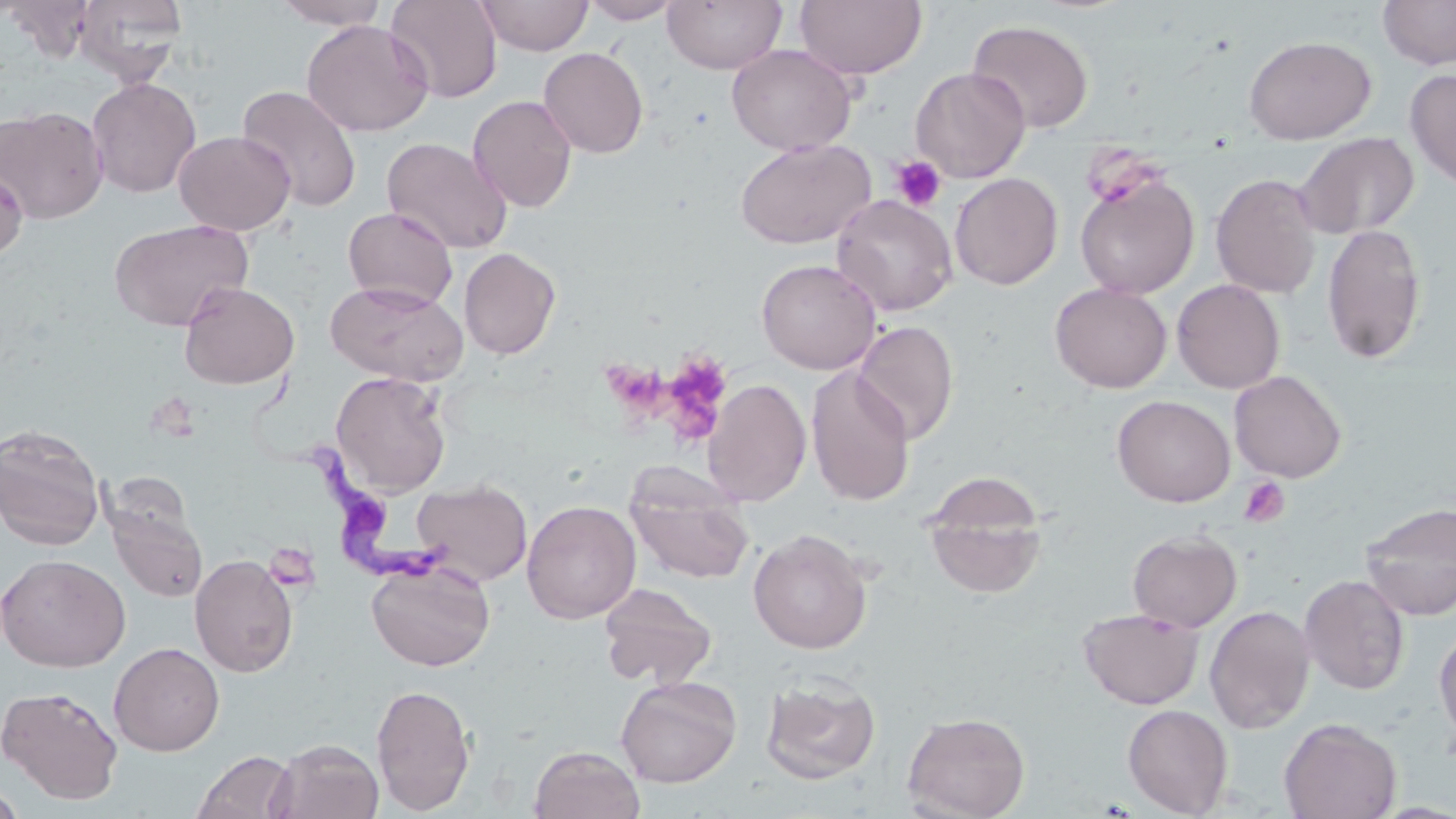 Approximate bounding boxes as [x1, y1, x2, y2] in pixels. Trypanosoma brucei locations: [257, 379, 454, 595]. Platelet locations: [1085, 137, 1160, 206], [890, 154, 948, 212], [655, 354, 734, 446], [615, 366, 680, 432], [1239, 476, 1290, 527], [265, 538, 322, 597]. Uninfected red blood cell locations: [3, 0, 98, 59], [74, 0, 188, 86], [273, 0, 389, 29], [385, 0, 502, 103], [475, 0, 593, 56], [581, 0, 683, 24], [662, 0, 787, 74], [795, 0, 927, 80], [1378, 0, 1456, 69], [301, 19, 433, 137], [967, 19, 1094, 133], [1243, 35, 1377, 144], [727, 43, 857, 155], [538, 47, 649, 158], [910, 66, 1030, 182], [1405, 69, 1456, 191], [86, 77, 201, 198], [237, 84, 362, 213], [468, 95, 577, 213], [0, 105, 109, 224], [174, 130, 295, 235], [1295, 131, 1419, 240], [382, 136, 512, 254], [735, 138, 876, 249], [0, 167, 28, 261], [1075, 171, 1199, 300], [950, 173, 1063, 290], [1211, 173, 1322, 299], [831, 194, 958, 316], [342, 206, 458, 310], [109, 219, 252, 331], [1321, 223, 1427, 364], [459, 247, 561, 360], [756, 258, 882, 374], [1172, 279, 1286, 394], [179, 281, 299, 389], [325, 281, 467, 386], [1050, 282, 1172, 393], [853, 320, 959, 444], [806, 366, 914, 507], [1229, 370, 1347, 483], [331, 371, 451, 498], [702, 378, 812, 506], [1112, 395, 1235, 507], [0, 423, 106, 550], [626, 465, 755, 586], [922, 473, 1049, 598], [411, 478, 532, 586], [521, 500, 640, 624], [1359, 502, 1456, 620], [106, 503, 207, 603], [748, 529, 871, 654], [1127, 530, 1241, 632], [0, 553, 130, 672], [189, 554, 298, 677], [366, 558, 496, 671], [1299, 574, 1410, 695], [598, 582, 718, 690], [1204, 605, 1315, 734], [1078, 608, 1204, 710], [1434, 626, 1456, 745], [109, 642, 225, 756], [761, 674, 880, 785], [615, 675, 741, 787], [371, 682, 476, 815], [0, 684, 124, 803], [1122, 704, 1233, 817], [902, 711, 1030, 819], [1279, 717, 1402, 819], [269, 738, 384, 819], [529, 745, 645, 819], [192, 751, 298, 819], [0, 784, 27, 818]. Slide-level diagnosis: Trypanosoma brucei. 1000x magnification. Single field of view. Thin blood film. Optical microscopy. May-Grünwald-Giemsa-stained preparation. Image is 1456×819 pixels.